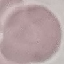

Malaria status: uninfected. Photographed with a smartphone camera at the microscope eyepiece. Automatically extracted cell patch, resized to 64 × 64 pixels. Giemsa-stained preparation. Thin smear of blood.